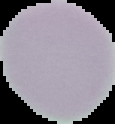

Summary:
  - Preparation: thin blood smear
  - Image size: 115×124 pixels
  - Result: no Plasmodium parasites seen
  - Image type: segmented cell region on a black background